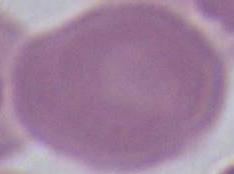

Captured at 1000x magnification. A red blood cell is seen. Micrograph.